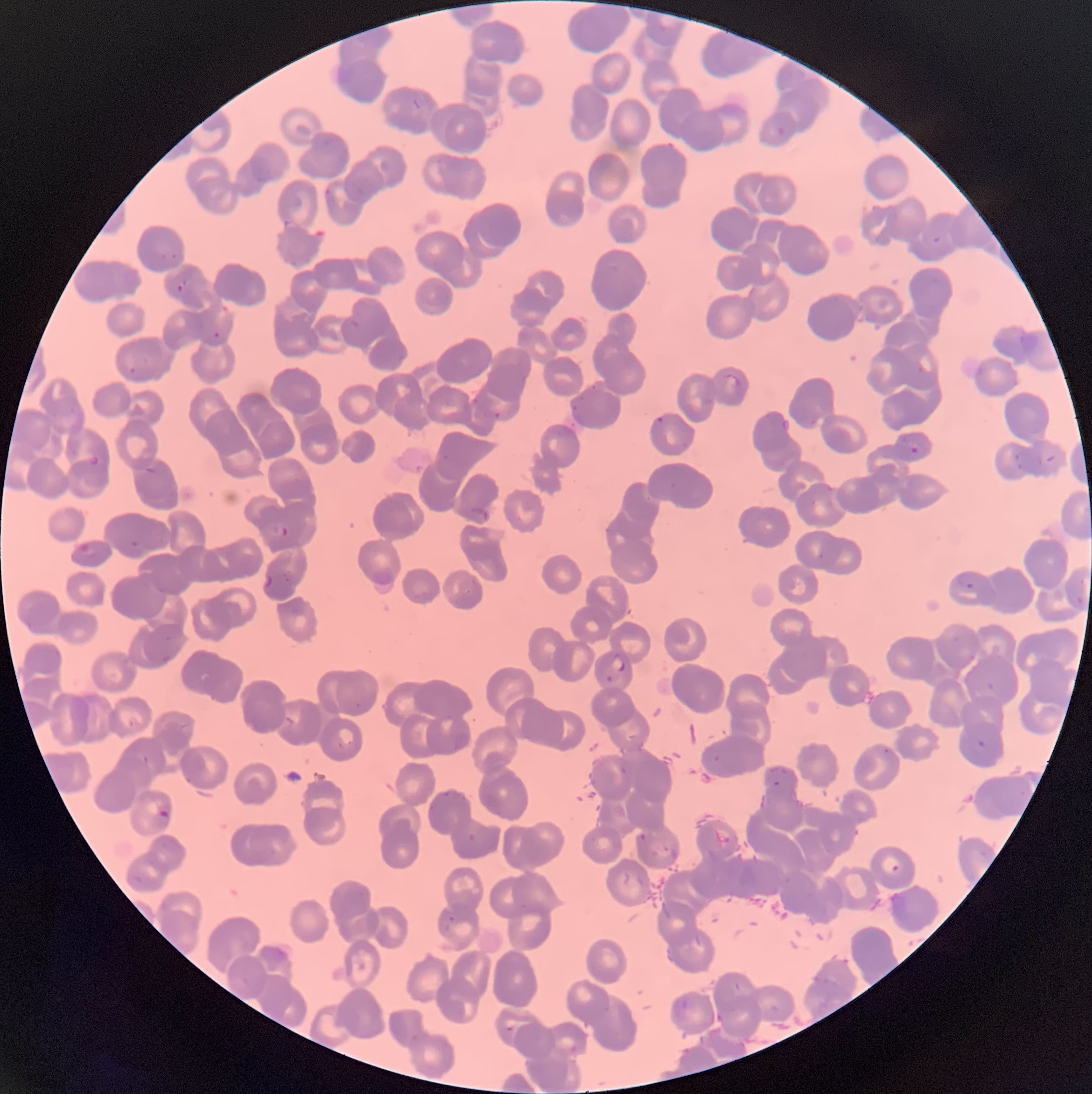
Summary:
  - Coordinate format: approximate bounding boxes as (x1, y1, x2, y2) in pixels
  - Plasmodium parasite locations: (776, 125, 786, 138), (249, 156, 272, 185), (324, 187, 336, 212), (282, 218, 299, 231), (933, 236, 941, 244), (159, 251, 179, 262), (177, 279, 187, 293), (346, 318, 360, 331), (213, 330, 221, 339), (1017, 332, 1039, 354), (129, 367, 136, 375), (722, 375, 740, 394), (589, 383, 599, 392), (569, 393, 585, 412), (471, 397, 479, 405), (492, 410, 502, 419), (651, 414, 665, 434), (780, 417, 791, 434), (808, 417, 819, 428), (910, 447, 919, 454), (1038, 448, 1058, 466), (87, 453, 100, 466), (1014, 454, 1023, 472), (142, 466, 157, 475), (824, 483, 834, 493), (809, 498, 817, 509), (471, 505, 489, 523), (268, 521, 291, 540), (130, 540, 140, 549), (77, 542, 97, 558), (264, 571, 274, 589), (956, 572, 976, 592), (1077, 594, 1083, 604), (611, 653, 627, 674), (605, 674, 614, 683), (986, 681, 994, 690), (336, 727, 356, 752), (883, 747, 891, 754), (140, 753, 150, 766), (710, 753, 725, 767), (184, 775, 195, 787), (773, 780, 781, 787), (1019, 789, 1026, 797), (157, 808, 170, 820), (468, 832, 476, 842), (636, 832, 654, 843), (880, 855, 902, 875), (132, 875, 143, 884), (889, 891, 909, 916), (443, 915, 455, 932), (261, 944, 290, 975), (667, 995, 694, 1024), (570, 1044, 577, 1053)
  - Plasmodium parasites too small for a box (approximate centers as (x, y) in pixels): (981, 743), (509, 1028)
  - Red blood cell morphology: rouleaux formation
  - Modality: light microscopy
  - Preparation: thin blood smear
  - Image size: 1092×1094 pixels